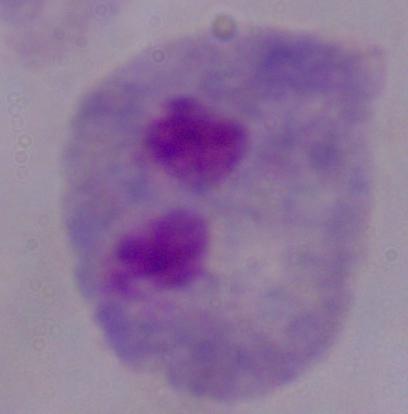

magnification = 1000x
modality = micrograph
identification = trichomonad